Report the malaria status of this cell.
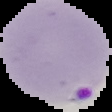
Parasitized.

Image is 112×112 pixels. From a thin blood film. The area outside the segmented cell region is set to black.